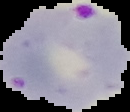
Summary:
  - Image size: 130×112 pixels
  - Image type: segmented cell region with the area outside set to black
  - Preparation: thin blood smear
  - Malaria status: parasitized